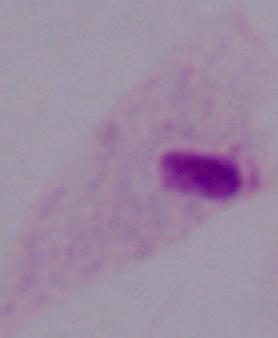

modality = micrograph
magnification = 1000x
identification = trichomonad